Outline each Plasmodium falciparum-infected red blood cell.
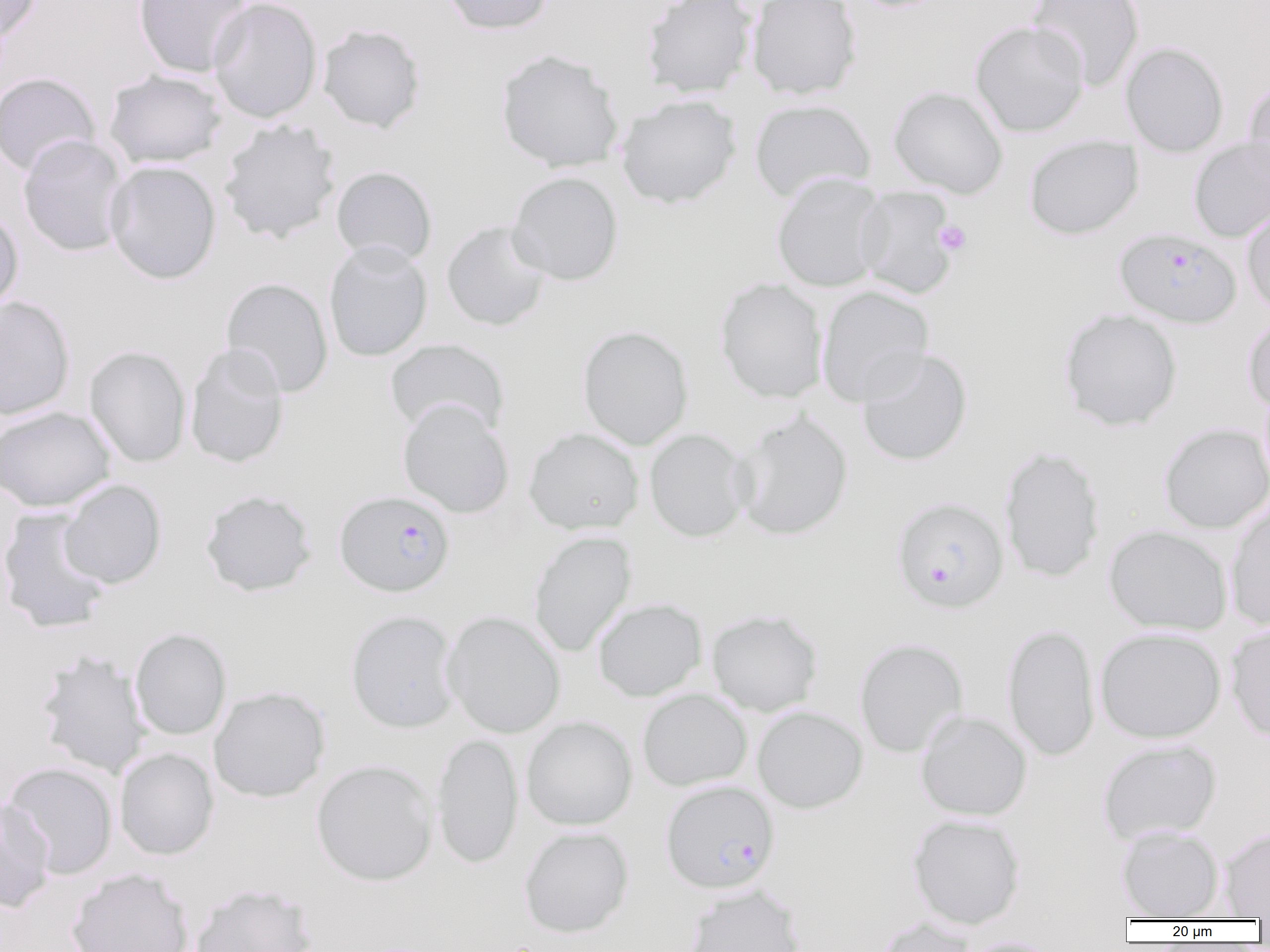
Approximate bounding boxes as (x1,y1)-(x2,y2) corner pairs in pixels.
Plasmodium falciparum-infected red blood cells: (1115,227)-(1241,328), (334,490)-(455,597), (891,496)-(1008,613), (660,780)-(779,893).

slide_level_diagnosis: Plasmodium falciparum
modality: light microscopy
uninfected_red_blood_cell_locations: 'approximate bounding boxes as (x1,y1)-(x2,y2) corner pairs in pixels: (0,0)-(43,44), (133,0)-(254,78), (208,0)-(323,123), (438,0)-(555,35), (641,0)-(757,98), (746,0)-(862,100), (1027,0)-(1146,91), (970,20)-(1089,137), (317,23)-(427,134), (1121,42)-(1229,157), (495,49)-(625,173), (104,70)-(227,169), (0,72)-(101,176), (1243,82)-(1270,187), (888,86)-(1008,198), (616,94)-(741,209), (748,99)-(877,204), (218,118)-(342,245), (18,134)-(129,257), (1023,134)-(1143,240), (1189,136)-(1270,242), (104,160)-(221,284), (331,166)-(437,267), (507,171)-(624,285), (770,173)-(889,292), (854,186)-(959,300), (1242,204)-(1270,318), (0,206)-(23,317), (441,220)-(552,332), (323,240)-(433,362), (220,276)-(333,398), (715,278)-(828,403), (816,285)-(934,407), (0,296)-(75,421), (1058,308)-(1183,432), (1243,315)-(1270,415), (576,325)-(694,450), (385,339)-(510,439), (184,344)-(290,469), (84,345)-(192,468), (856,348)-(973,467), (397,399)-(515,519), (0,406)-(115,511), (730,410)-(853,541), (1158,422)-(1270,533), (523,427)-(644,535), (644,429)-(751,542), (999,445)-(1105,583), (59,479)-(167,589), (200,490)-(317,597), (1225,499)-(1270,631), (0,508)-(113,634), (1104,525)-(1233,636), (528,531)-(636,656), (593,598)-(707,701), (706,609)-(823,716), (345,610)-(461,733), (443,611)-(566,738), (1226,622)-(1270,742), (1002,624)-(1100,762), (1095,627)-(1226,743), (131,628)-(231,740), (854,637)-(969,758), (35,649)-(151,778), (208,686)-(330,802), (637,689)-(752,791), (752,705)-(868,813), (915,710)-(1032,821), (521,716)-(637,830), (431,732)-(524,869), (1097,739)-(1222,845), (114,747)-(219,860), (312,759)-(438,886), (2,762)-(119,880), (0,796)-(55,913), (907,813)-(1025,929), (1116,825)-(1224,919), (519,826)-(634,937), (1218,826)-(1270,919), (67,867)-(194,952), (189,882)-(318,952), (684,884)-(805,952), (871,916)-(979,952), (959,937)-(1060,952)'
preparation: thin blood film
image_size: 1270×952 pixels
platelet_locations: 'approximate bounding boxes as (x1,y1)-(x2,y2) corner pairs in pixels: (934,220)-(972,256)'
field_of_view: single
magnification: 1000x